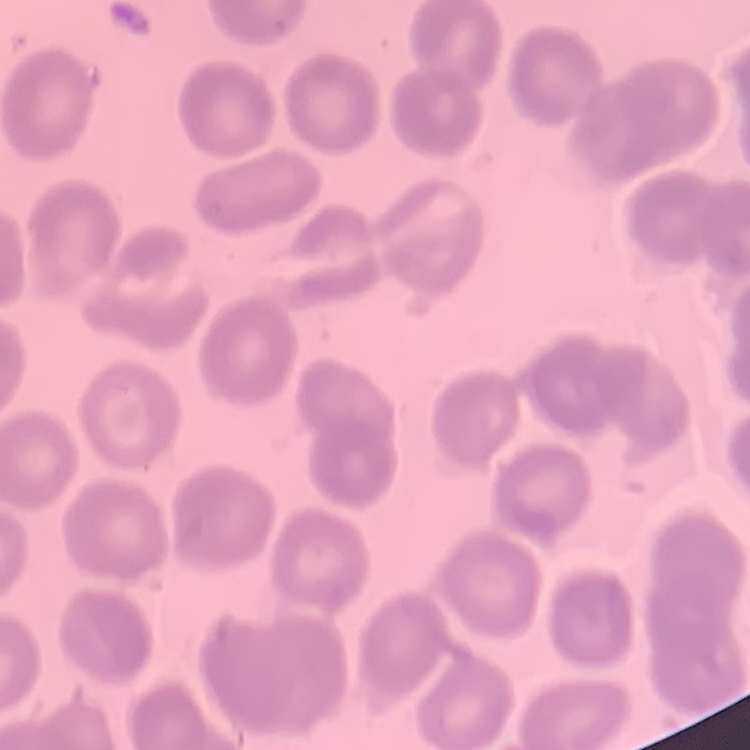
Summary:
  - Erythrocyte morphology: no rouleaux formation
  - Stain: Field's or Giemsa
  - Image type: square crop of a larger photomicrograph
  - Preparation: thin peripheral smear